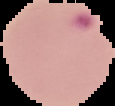
Summary:
  - Image type: segmented cell region with the area outside set to black
  - Preparation: thin blood film
  - Image size: 115×106 pixels
  - Malaria status: parasitized